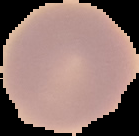
Summary:
  - Malaria status: uninfected
  - Preparation: thin blood smear
  - Image type: segmented cell region with the area outside set to black
  - Image size: 139×136 pixels